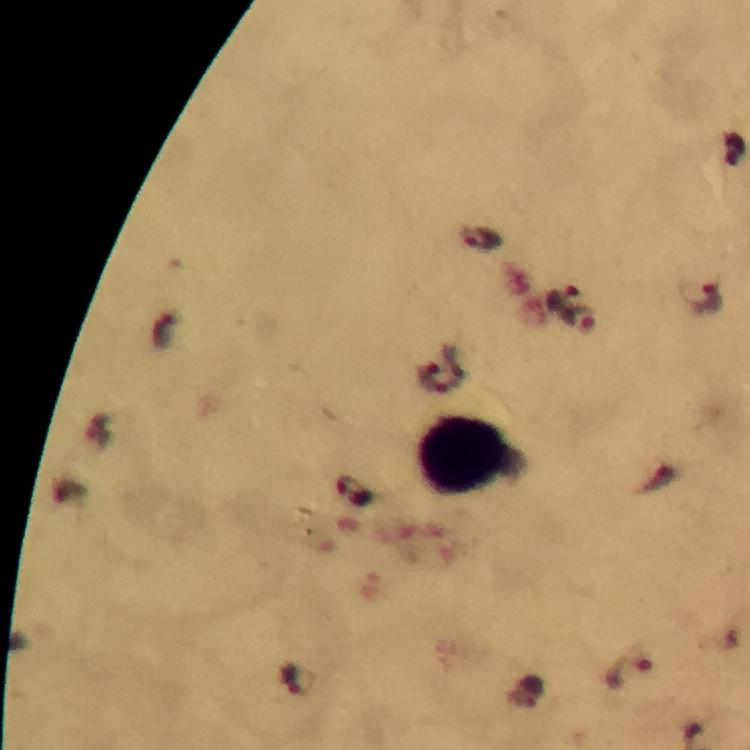
Approximate centers as {x, y} in pixels. Malaria parasite locations: {482, 240}, {563, 298}, {707, 299}, {580, 319}, {352, 491}, {630, 673}, {298, 681}. Leukocyte locations: {464, 454}. Photographed with a smartphone mounted on the microscope. A crop from one field of view. Thick blood film. Immersion oil applied. Image is 750×750 pixels. At 100x magnification. Giemsa stain. From a malaria diagnostic workup.